Outline each uninfected red blood cell.
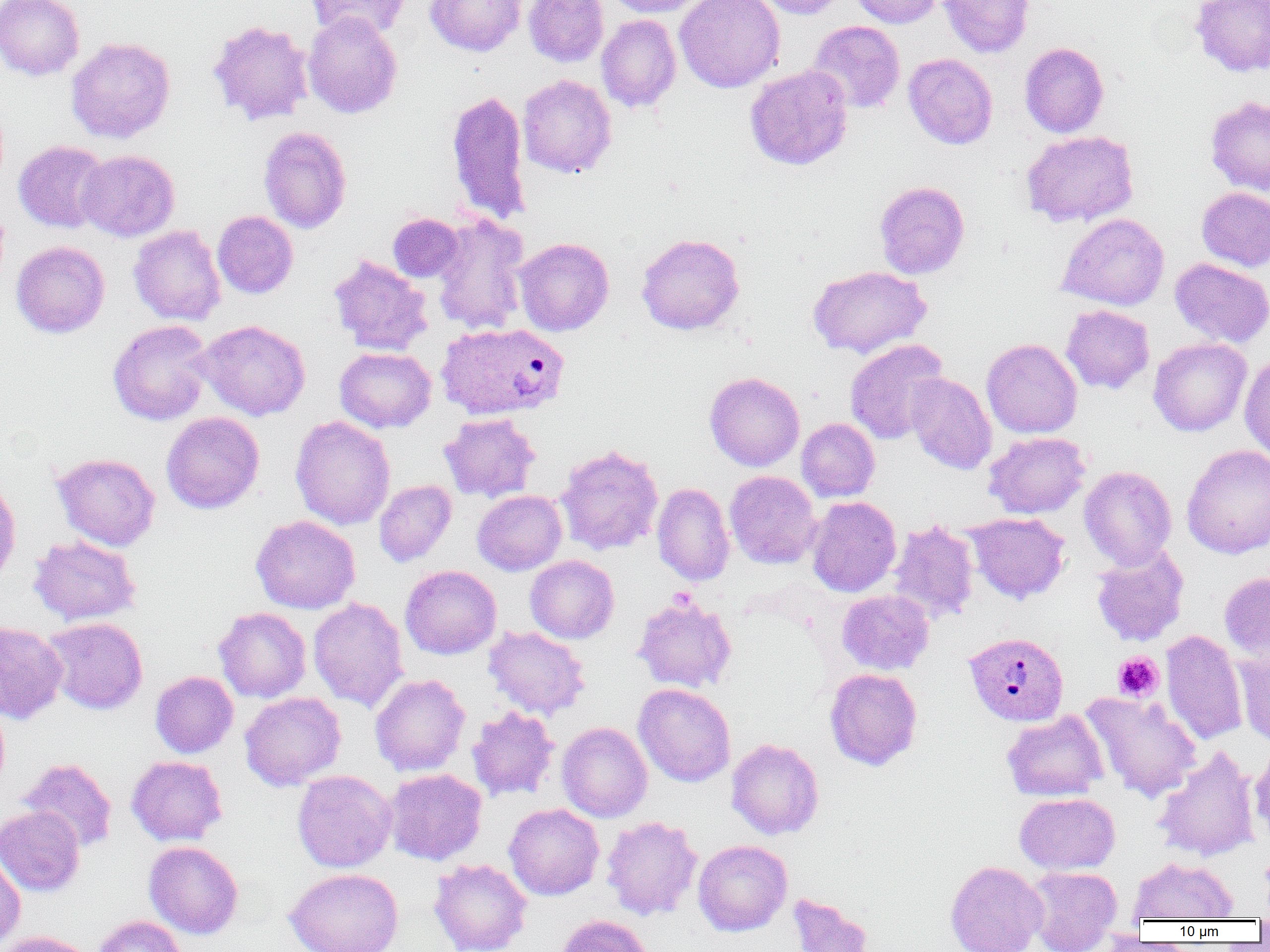

Approximate bounding boxes as (x1,y1)-(x2,y2) corner pairs in pixels.
Uninfected red blood cells: (0,0)-(85,81), (305,0)-(411,41), (426,0)-(525,56), (524,0)-(608,67), (606,0)-(710,17), (674,0)-(785,93), (753,0)-(849,19), (849,0)-(944,28), (939,0)-(1034,58), (1189,0)-(1270,78), (302,11)-(403,118), (596,15)-(681,113), (208,20)-(314,125), (807,20)-(905,114), (67,37)-(175,143), (1019,42)-(1109,138), (903,53)-(998,149), (745,65)-(853,171), (517,74)-(617,178), (445,88)-(531,225), (1205,95)-(1270,196), (258,126)-(352,233), (1021,131)-(1138,228), (13,141)-(109,232), (76,150)-(180,241), (874,181)-(970,279), (1197,187)-(1270,272), (213,211)-(298,299), (387,213)-(464,282), (431,213)-(530,335), (1057,213)-(1170,310), (366,217)-(456,317), (129,225)-(226,326), (636,233)-(744,335), (514,237)-(614,336), (11,241)-(109,338), (328,255)-(433,356), (1170,258)-(1270,347), (808,265)-(932,358), (1061,305)-(1154,394), (108,320)-(214,425), (194,320)-(311,420), (1148,337)-(1252,436), (844,338)-(949,444), (981,338)-(1082,438), (335,347)-(436,433), (1240,353)-(1270,461), (704,372)-(805,471), (906,373)-(997,474), (161,412)-(264,514), (439,413)-(540,503), (290,415)-(395,530), (797,418)-(880,502), (983,432)-(1090,519), (555,444)-(664,555), (1182,445)-(1270,558), (52,453)-(160,551), (1079,465)-(1177,569), (725,471)-(821,569), (0,477)-(21,587), (374,480)-(456,567), (652,483)-(735,586), (472,490)-(567,575), (806,496)-(901,597), (964,513)-(1070,604), (251,515)-(360,614), (888,520)-(980,624), (28,535)-(141,626), (1090,545)-(1190,647), (525,555)-(619,644), (400,565)-(502,659), (1219,572)-(1270,662), (837,589)-(934,675), (633,595)-(737,692), (308,597)-(409,712), (213,607)-(311,702), (42,617)-(148,714), (0,621)-(67,724), (484,626)-(590,720), (1161,630)-(1247,745), (1235,647)-(1270,748), (824,668)-(922,771), (150,671)-(238,758), (370,673)-(471,777), (633,683)-(736,787), (1082,691)-(1202,801), (240,692)-(346,790), (0,699)-(10,796), (467,707)-(559,802), (1002,709)-(1108,801), (557,721)-(652,822), (726,738)-(824,839), (1249,743)-(1270,845), (1153,746)-(1260,862), (126,755)-(227,846), (18,758)-(117,853), (383,768)-(487,865), (292,770)-(397,872), (1014,793)-(1120,874), (504,803)-(604,900), (0,806)-(85,896), (601,815)-(702,920), (693,839)-(792,936), (144,841)-(243,939), (0,850)-(26,950), (1128,856)-(1237,922), (429,858)-(532,952), (945,860)-(1047,952), (1023,865)-(1123,952), (284,868)-(404,952), (787,892)-(874,952), (555,914)-(654,952), (92,915)-(188,952), (1255,918)-(1270,941), (0,930)-(97,952).

Platelet locations: (1112,652)-(1163,701). Plasmodium vivax-infected red blood cell locations: (436,322)-(570,420), (964,631)-(1069,726). Slide-level diagnosis: Plasmodium vivax. Image is 1270×952 pixels. Captured at 1000x magnification. Single field of view. Thin blood film. Light microscopy.